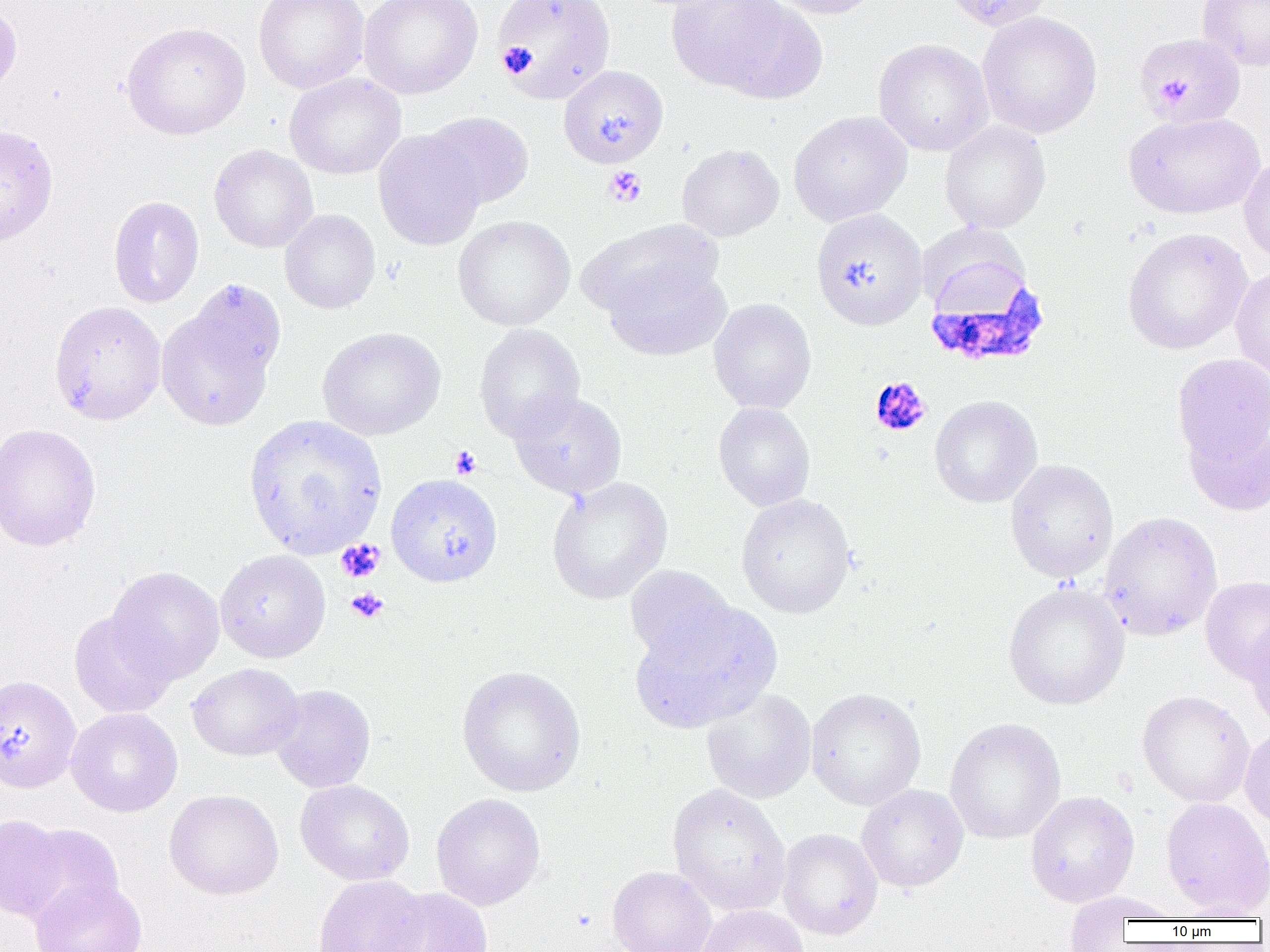

Approximate bounding boxes as [x1, y1, x2, y2] in pixels. Plasmodium falciparum-infected red blood cell locations: [923, 258, 1051, 370]. Uninfected red blood cell locations: [254, 0, 370, 93], [358, 0, 483, 99], [494, 0, 616, 104], [760, 0, 881, 19], [942, 0, 1055, 31], [1196, 0, 1269, 71], [667, 1, 822, 100], [0, 4, 22, 101], [977, 11, 1102, 139], [121, 22, 251, 141], [1134, 33, 1245, 127], [873, 38, 994, 156], [558, 65, 668, 168], [284, 73, 406, 179], [421, 111, 535, 210], [788, 111, 913, 226], [1124, 111, 1265, 220], [939, 120, 1051, 234], [0, 124, 59, 247], [373, 129, 485, 251], [676, 143, 784, 242], [209, 145, 318, 253], [1238, 154, 1270, 264], [108, 195, 204, 308], [810, 208, 928, 330], [280, 209, 381, 314], [453, 215, 575, 331], [578, 218, 723, 323], [1122, 227, 1253, 355], [603, 261, 732, 361], [1230, 264, 1270, 383], [708, 297, 817, 414], [48, 300, 167, 425], [156, 303, 278, 431], [473, 323, 585, 443], [317, 326, 445, 441], [1172, 354, 1270, 467], [509, 390, 628, 500], [930, 395, 1043, 508], [713, 402, 816, 512], [244, 413, 388, 560], [1183, 416, 1270, 516], [0, 422, 101, 553], [1004, 458, 1119, 583], [385, 473, 503, 587], [546, 476, 673, 605], [735, 493, 857, 619], [1099, 511, 1222, 641], [215, 549, 330, 663], [624, 565, 736, 666], [106, 566, 225, 683], [1200, 576, 1270, 684], [1003, 582, 1130, 710], [630, 600, 781, 732], [69, 610, 178, 718], [1245, 620, 1270, 729], [187, 663, 303, 761], [456, 664, 587, 798], [0, 674, 82, 793], [268, 684, 376, 793], [805, 687, 926, 811], [701, 688, 817, 804], [1137, 690, 1254, 808], [66, 708, 183, 816], [944, 717, 1066, 845], [1240, 727, 1270, 832], [294, 779, 415, 886], [668, 783, 791, 915], [856, 784, 968, 893], [164, 789, 284, 899], [1025, 790, 1139, 907], [431, 792, 546, 911], [1161, 797, 1270, 917], [0, 813, 73, 923], [14, 821, 124, 926], [776, 828, 882, 940], [607, 866, 717, 952], [311, 874, 428, 952], [30, 878, 148, 952], [377, 887, 493, 952], [1061, 890, 1183, 942], [695, 904, 808, 952], [1172, 904, 1268, 922]. Platelet locations: [498, 43, 537, 76], [1165, 75, 1193, 104], [603, 166, 647, 207], [869, 376, 932, 437], [448, 445, 482, 479], [336, 539, 384, 583], [346, 587, 388, 623]. Slide-level diagnosis: Plasmodium falciparum. One field of a larger specimen. Thin blood smear. Image is 1270×952 pixels. Optical microscopy. Captured at 1000x magnification.